Report the malaria status of this cell.
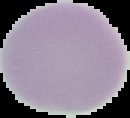

It is uninfected.

Image is 130×118 pixels. Cell region segmented out of the field of view; the surrounding area is masked to black. From a thin blood smear.